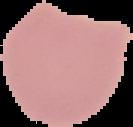 Image is 133×127 pixels. Segmented cell region on a black background. Malaria status: uninfected. From a thin blood smear.